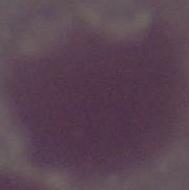

modality = micrograph
identification = erythrocyte
magnification = 1000x